Report the malaria status of this cell.
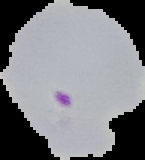

It is parasitized.

The area outside the segmented cell region is set to black. Image is 145×160 pixels. From a thin blood film.